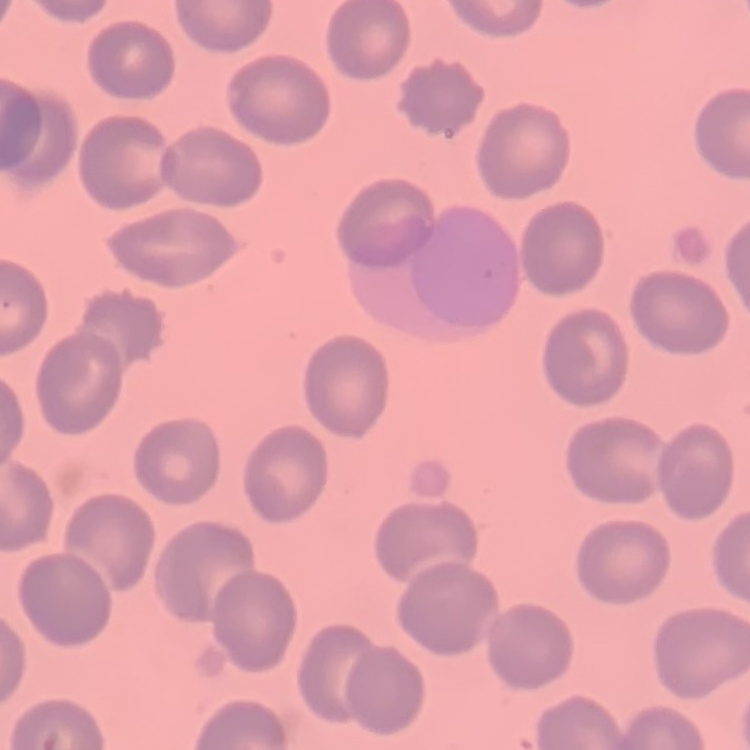
Summary:
  - Red blood cell morphology: no rouleaux formation
  - Image type: one tile cut from a larger photomicrograph
  - Stain: Field's or Giemsa
  - Preparation: thin peripheral smear